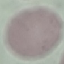
Summary:
  - Result: no malaria parasites detected
  - Preparation: thin smear
  - Image type: cell patch, automatically extracted from a larger field of view and resized to 64 × 64 pixels
  - Stain: Giemsa
  - Capture: smartphone camera at the microscope eyepiece